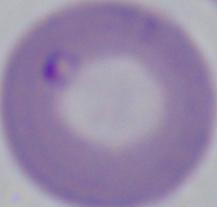

A Babesia parasite is seen. Micrograph. Captured at 1000x magnification.